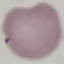

Malaria status: uninfected. Thin blood film. Automatically extracted cell patch, resized to 64 × 64 pixels. Photographed with a smartphone camera at the microscope eyepiece. Giemsa stain.